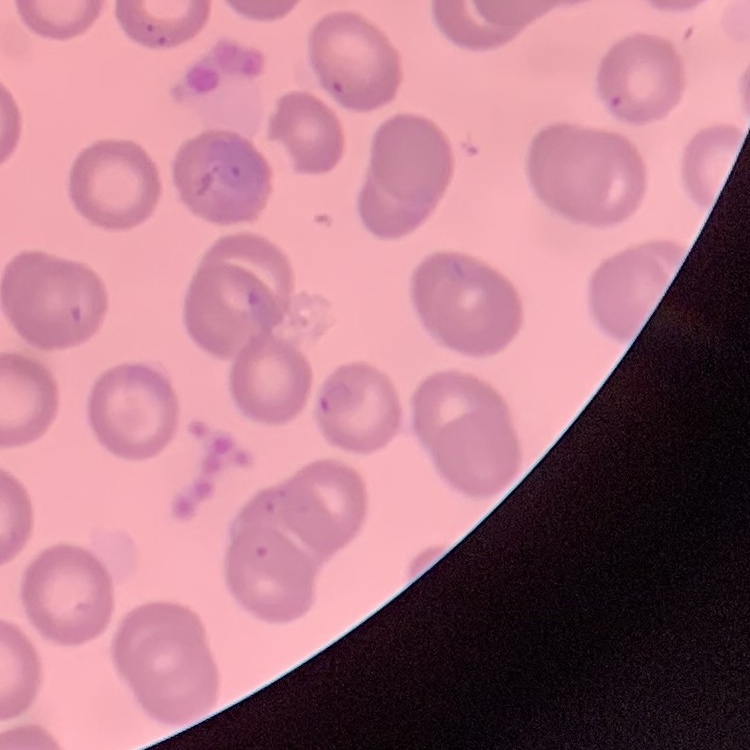

Summary:
  - Erythrocyte morphology: no rouleaux formation
  - Image type: square crop of a larger photomicrograph
  - Stain: Field's or Giemsa
  - Preparation: thin blood smear